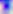

Summary:
  - Modality: micrograph
  - Identification: Toxoplasma gondii
  - Magnification: 400x